Assess this cell for malaria.
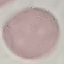

Uninfected.

image type = automatically extracted cell patch, resized to 64 × 64 pixels
capture = smartphone through the microscope eyepiece
stain = Giemsa
preparation = thin blood film